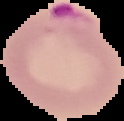

Summary:
  - Malaria status: parasitized
  - Preparation: thin blood smear
  - Image type: segmented cell region on a black background
  - Image size: 124×121 pixels